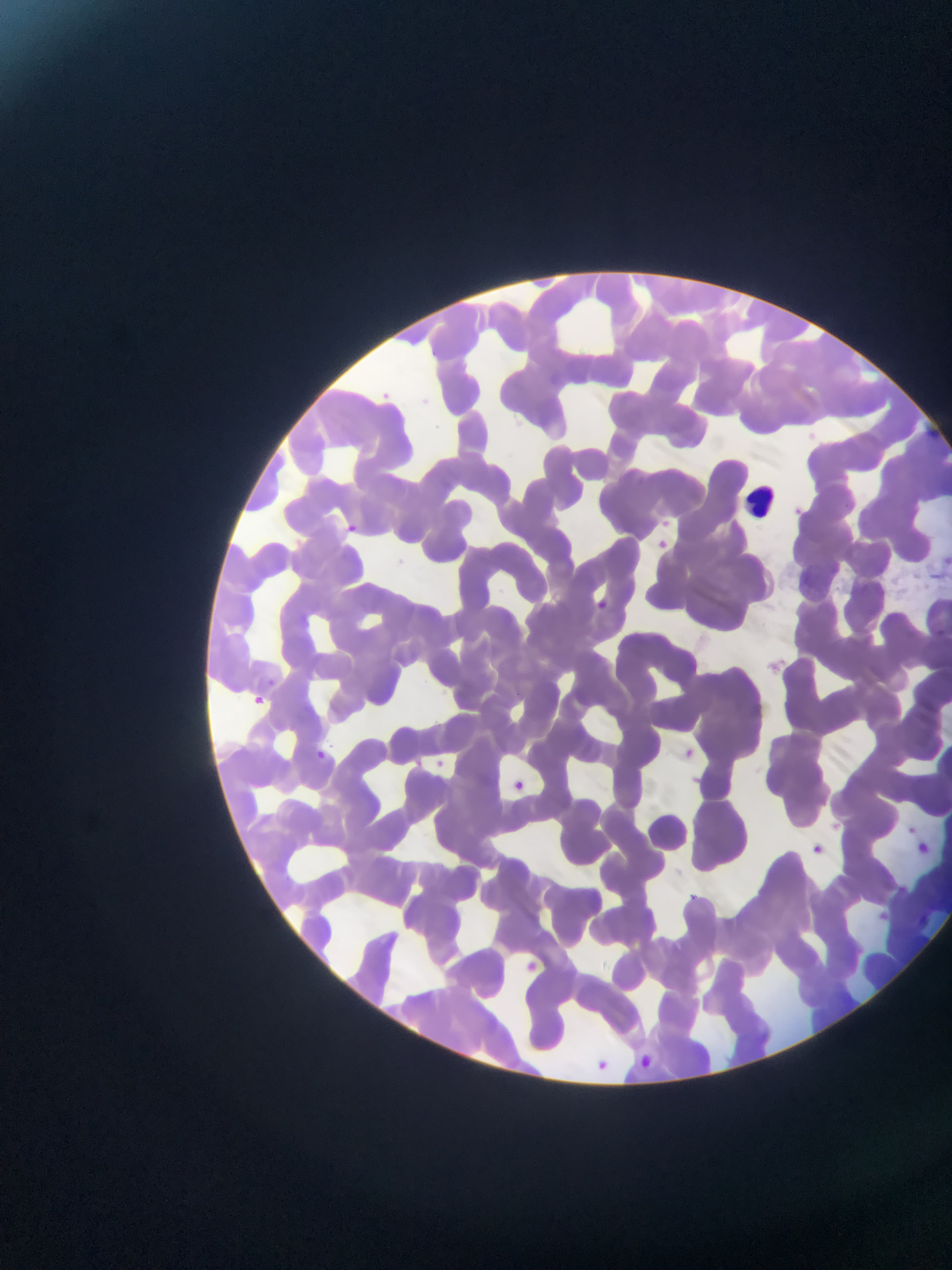

leukocyte locations = approximate bounding boxes as [left, top, right, bottom] in pixels: [744, 482, 782, 520]
capture = mobile-phone photograph through a microscope
image size = 952×1270 pixels
Plasmodium parasite locations = approximate bounding boxes as [left, top, right, bottom] in pixels: [418, 386, 443, 422], [375, 388, 398, 411], [919, 412, 944, 436], [832, 496, 854, 517], [789, 498, 800, 521], [657, 510, 695, 537], [348, 519, 356, 531], [655, 533, 675, 563], [591, 597, 617, 615], [933, 622, 950, 636], [260, 665, 285, 695], [251, 696, 270, 707], [679, 738, 701, 760], [314, 748, 339, 773], [424, 750, 452, 779], [509, 771, 538, 805], [832, 810, 841, 828], [899, 817, 921, 837], [908, 837, 935, 867], [810, 841, 825, 858], [896, 877, 916, 903], [684, 888, 708, 910], [881, 905, 891, 928], [911, 911, 926, 930], [519, 957, 544, 984], [628, 1051, 655, 1072], [591, 1056, 617, 1081]
field of view = single
preparation = thin blood film
country = Ghana